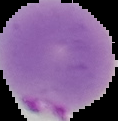
Result: Plasmodium parasites detected. The area outside the segmented cell region is set to black. From a thin blood smear. Image is 118×121 pixels.